Identify the preparation type.
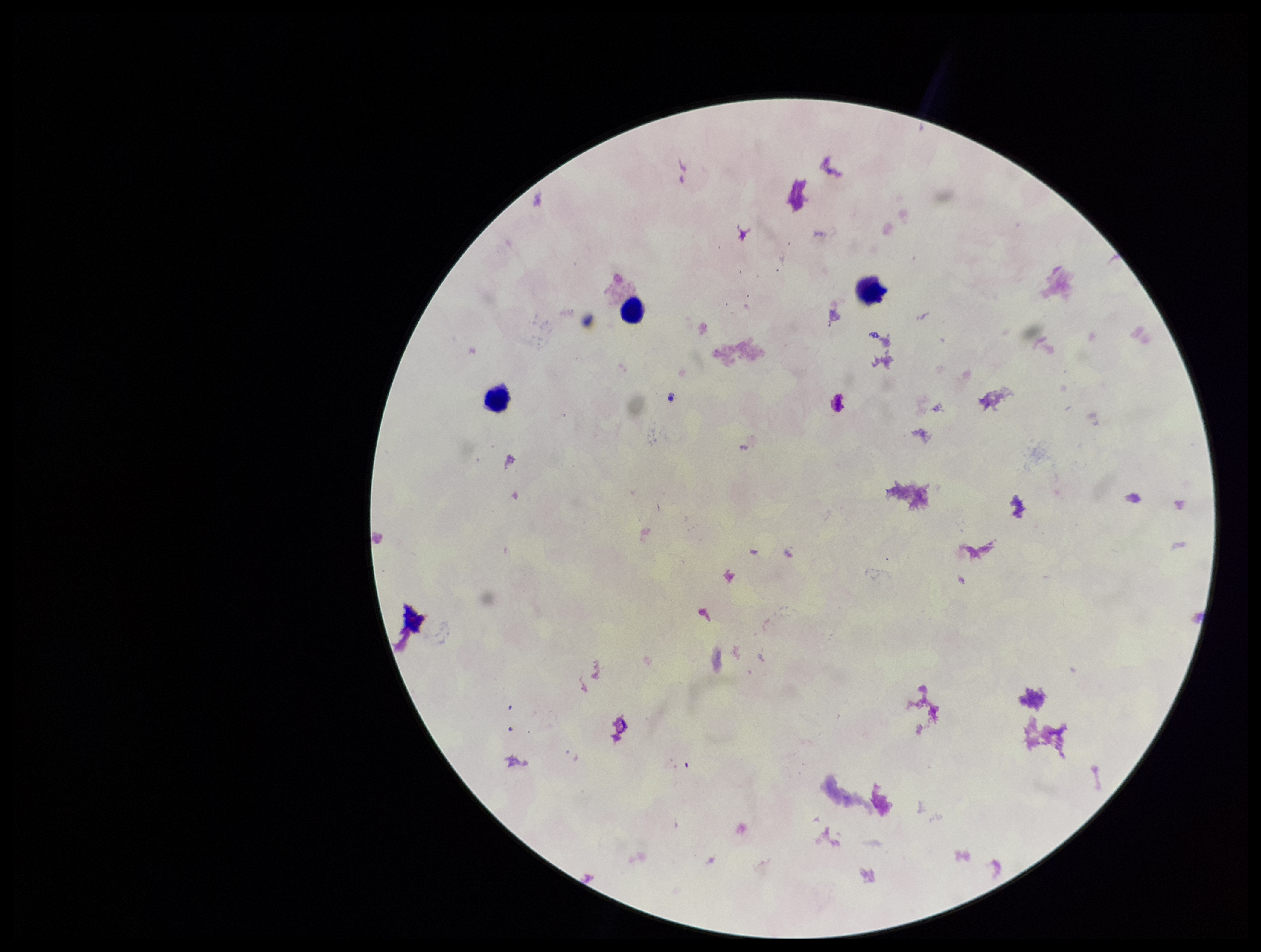

A thick smear.

plasmodium_parasites: none detected
stain: Giemsa
image_size: 1261×952 pixels
parasite_count: 0
patient_malaria_status: negative
field_of_view: single
capture: smartphone photograph through the microscope eyepiece
leukocyte_count: 3